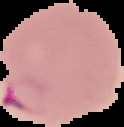

malaria status = parasitized
image type = cell region segmented out of the field of view; surrounding area masked to black
image size = 124×127 pixels
preparation = thin blood film